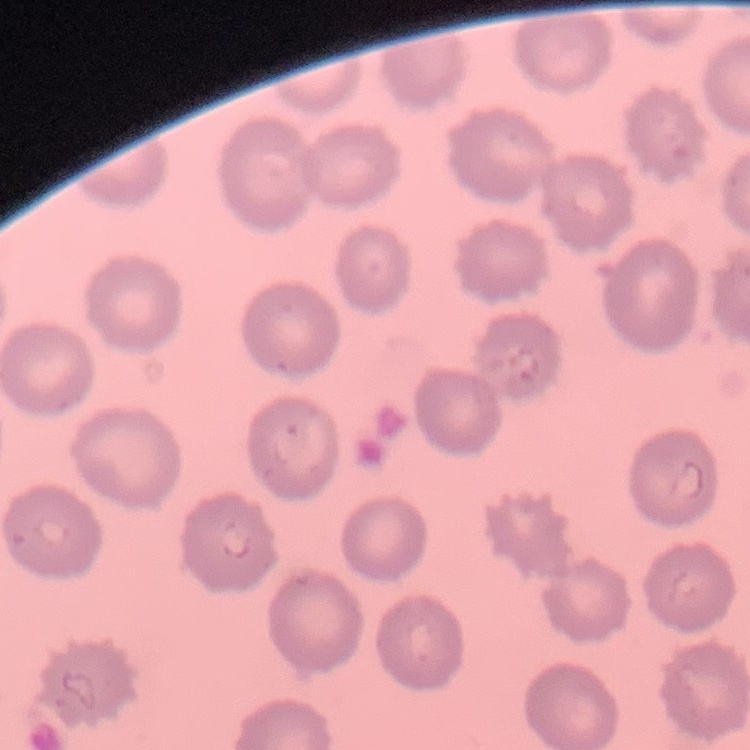

Summary:
  - Red blood cell morphology: no rouleaux formation
  - Stain: Field's or Giemsa
  - Image type: one tile cut from a larger photomicrograph
  - Preparation: thin blood smear